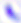
{
  "magnification": "400x",
  "identification": "Toxoplasma gondii",
  "modality": "micrograph"
}